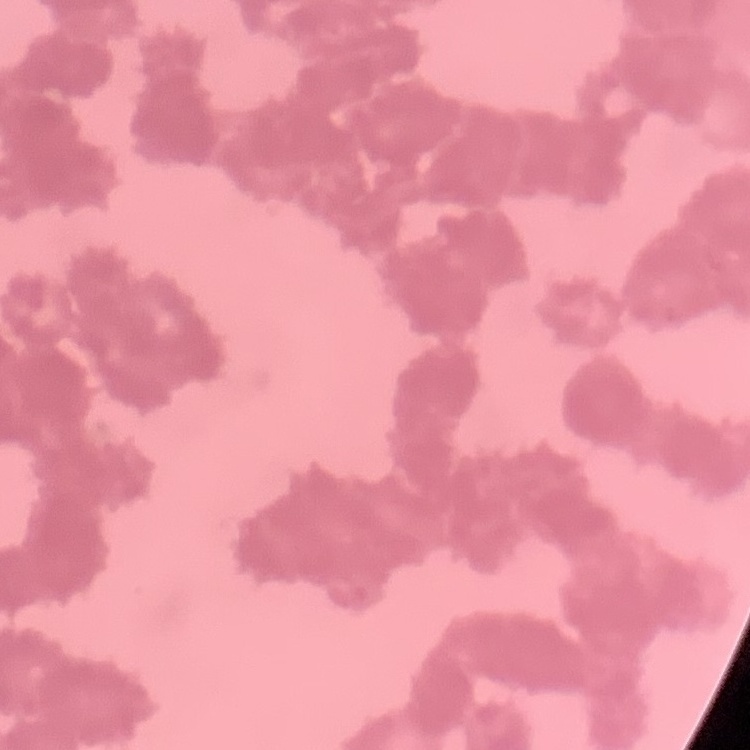
erythrocyte morphology = rouleaux formation
image type = one tile cut from a larger photomicrograph
stain = Field's or Giemsa
preparation = thin blood smear